Assess the morphology of the erythrocytes.
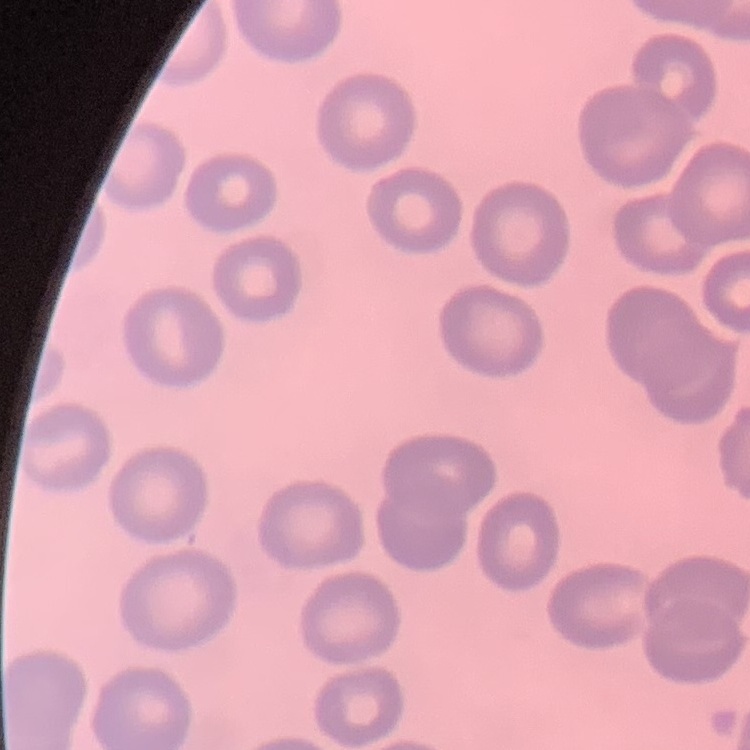

No rouleaux formation.

preparation = thin blood film
stain = Field's or Giemsa
image type = square crop of a larger photomicrograph